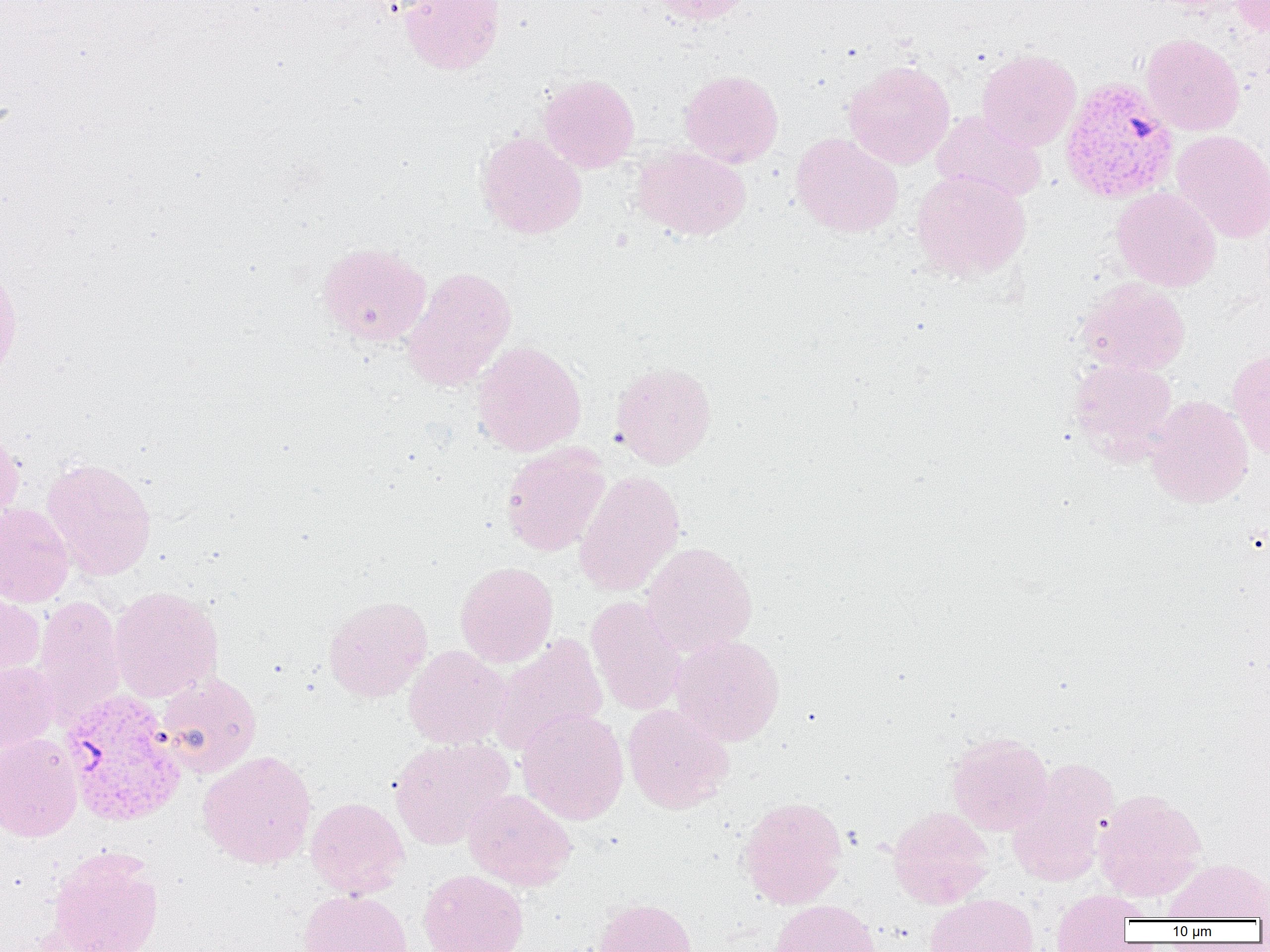

Summary:
  - Coordinate format: approximate bounding boxes as [x1, y1, x2, y2] in pixels
  - Uninfected red blood cell locations (subset): [399, 0, 506, 75], [651, 0, 752, 25], [1230, 0, 1270, 35], [1141, 33, 1244, 136], [977, 48, 1081, 151], [844, 59, 955, 169], [679, 69, 784, 168], [538, 73, 639, 173], [931, 110, 1047, 203], [1171, 130, 1270, 243], [476, 131, 587, 239], [791, 132, 904, 237], [633, 145, 751, 241], [911, 168, 1031, 281], [1112, 187, 1221, 291], [317, 242, 432, 346], [0, 262, 22, 384], [401, 266, 517, 392], [1077, 277, 1191, 376], [471, 340, 586, 457], [1227, 347, 1270, 457], [1069, 358, 1177, 458], [610, 361, 716, 469], [1146, 395, 1253, 507], [0, 426, 24, 530], [500, 444, 610, 556], [40, 457, 157, 581], [573, 471, 685, 597], [0, 503, 75, 607], [641, 542, 758, 657], [455, 561, 557, 668], [109, 585, 223, 702], [0, 589, 45, 684], [31, 595, 127, 727], [323, 595, 432, 702], [586, 596, 687, 716], [488, 633, 608, 756], [669, 634, 785, 746], [404, 645, 509, 749], [0, 661, 58, 754], [157, 671, 262, 778], [623, 704, 734, 814], [516, 707, 629, 825], [946, 731, 1053, 836], [0, 732, 83, 842], [389, 736, 515, 850], [197, 751, 317, 869], [1007, 758, 1118, 886], [463, 788, 577, 891], [1094, 788, 1206, 901], [739, 795, 847, 909], [306, 797, 409, 898], [888, 805, 994, 909], [46, 847, 165, 952], [1165, 858, 1270, 922], [418, 869, 529, 952], [298, 889, 413, 952], [1051, 890, 1141, 951], [924, 893, 1039, 952], [593, 897, 698, 952], [769, 899, 882, 952]
  - Plasmodium vivax-infected red blood cell locations (subset): [58, 689, 187, 827]
  - Slide-level diagnosis: Plasmodium vivax
  - Preparation: thin blood film
  - Modality: optical microscopy
  - Image size: 1270×952 pixels
  - Magnification: 1000x
  - Field of view: one of a larger specimen